Evaluate for malaria.
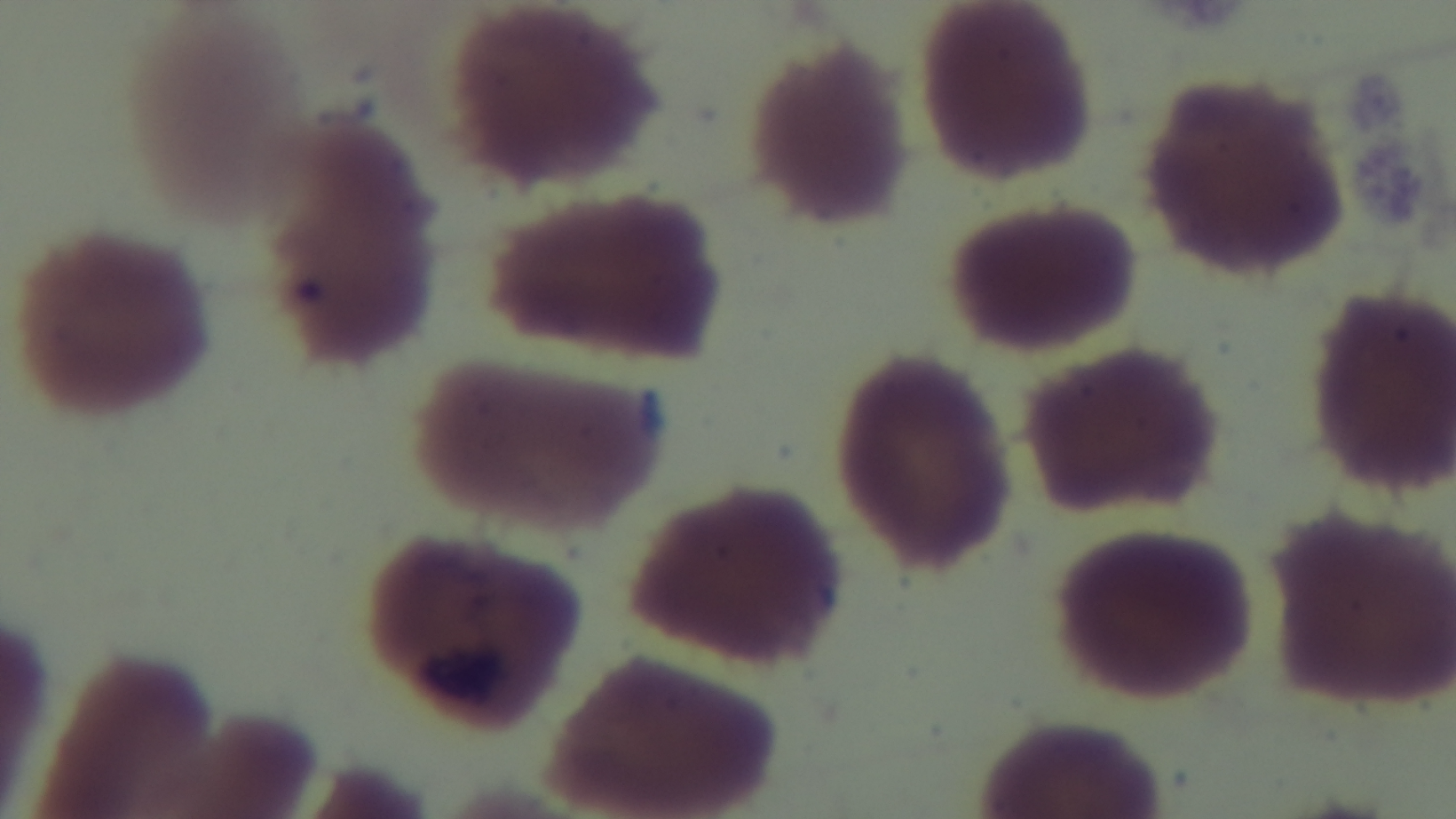
Uninfected.

Giemsa-stained. Mounted 4K digital camera. Preparation: thin. One field from the slide. Oil-immersion objective, 100x. Light microscopy.